State which cell type is depicted.
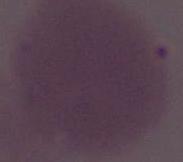
An erythrocyte.

modality: micrograph
magnification: 1000x